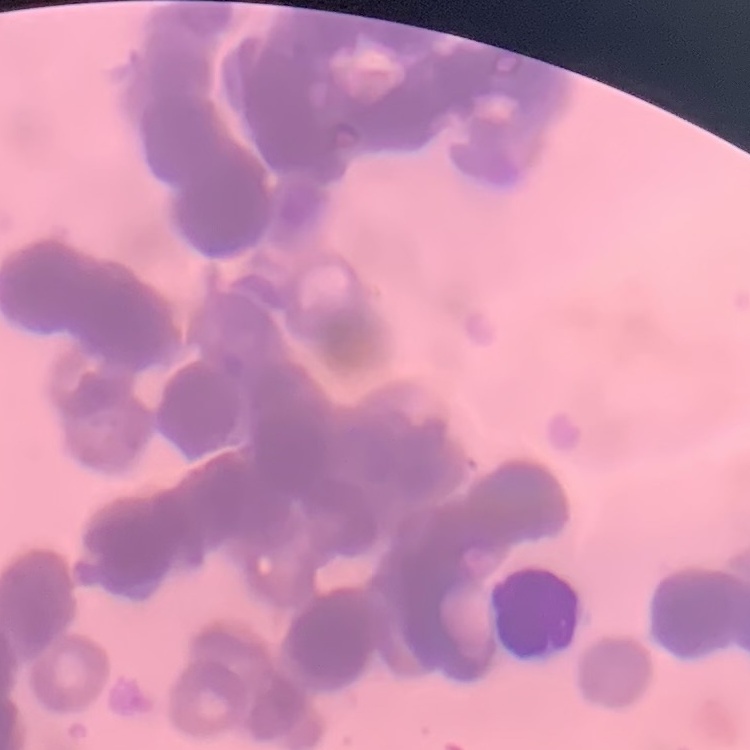

Summary:
  - Red blood cell morphology: rouleaux formation
  - Preparation: thin blood film
  - Stain: Field's or Giemsa
  - Image type: one tile cut from a larger photomicrograph